State which parasite is depicted.
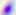
This is Toxoplasma gondii.

magnification = 400x
modality = photomicrograph